State which cell type is depicted.
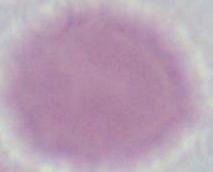

An erythrocyte.

magnification = 1000x
modality = photomicrograph